Point out each Plasmodium parasite.
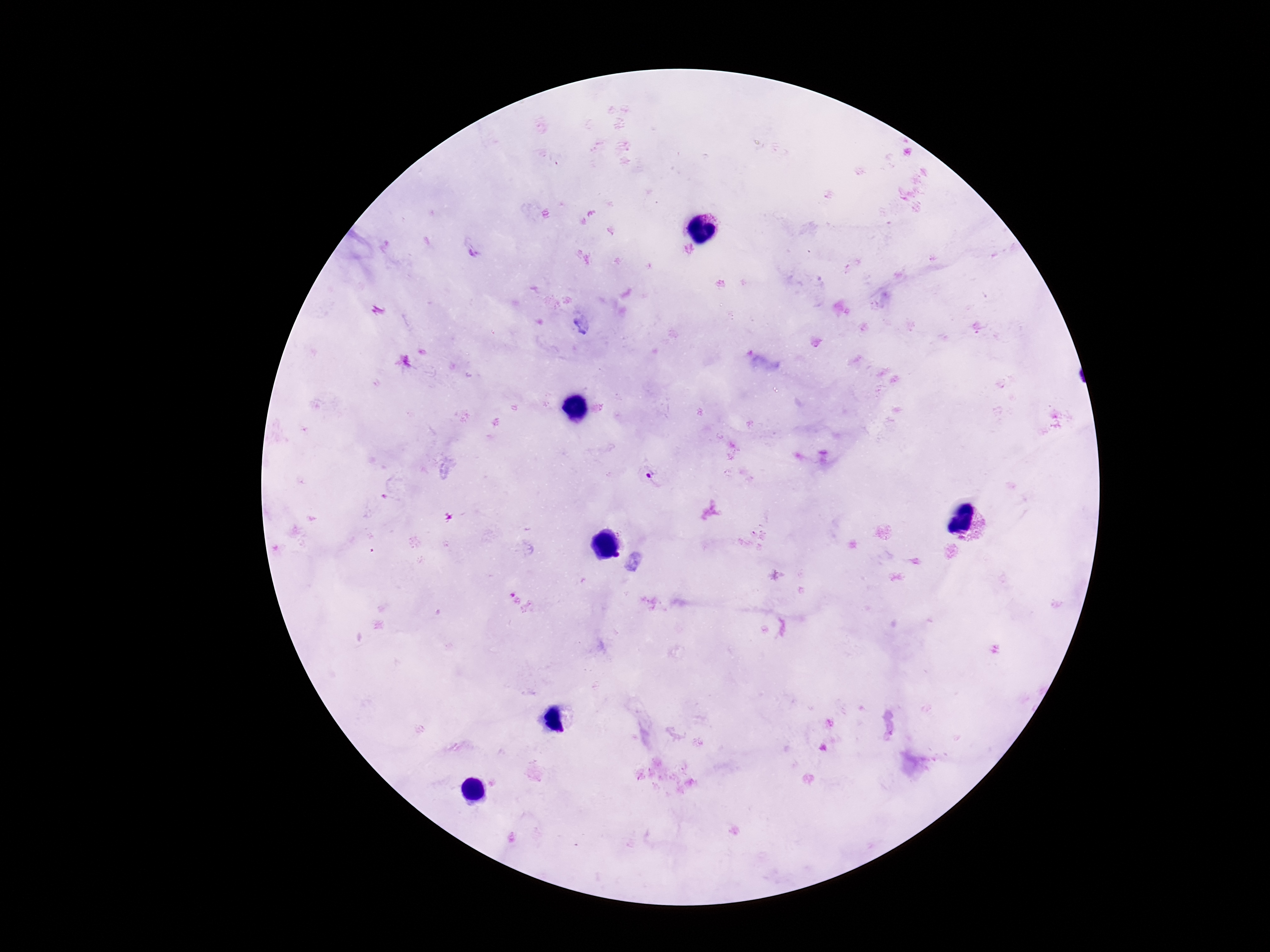

Approximate object centers, in pixels from the top-left corner.
Plasmodium parasites: (x=649, y=475).

{
  "image_size": "1270×952 pixels",
  "magnification": "100x",
  "patient_malaria_status": "positive",
  "field_of_view": "single",
  "capture": "smartphone camera through the microscope eyepiece",
  "preparation": "thick peripheral-blood smear",
  "stain": "Giemsa"
}